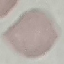 Malaria status: uninfected. Acquired by smartphone through the microscope eyepiece. Giemsa stain. Thin blood film. Automatically extracted cell patch, resized to 64 × 64 pixels.